Locate every leukocyte (white blood cell).
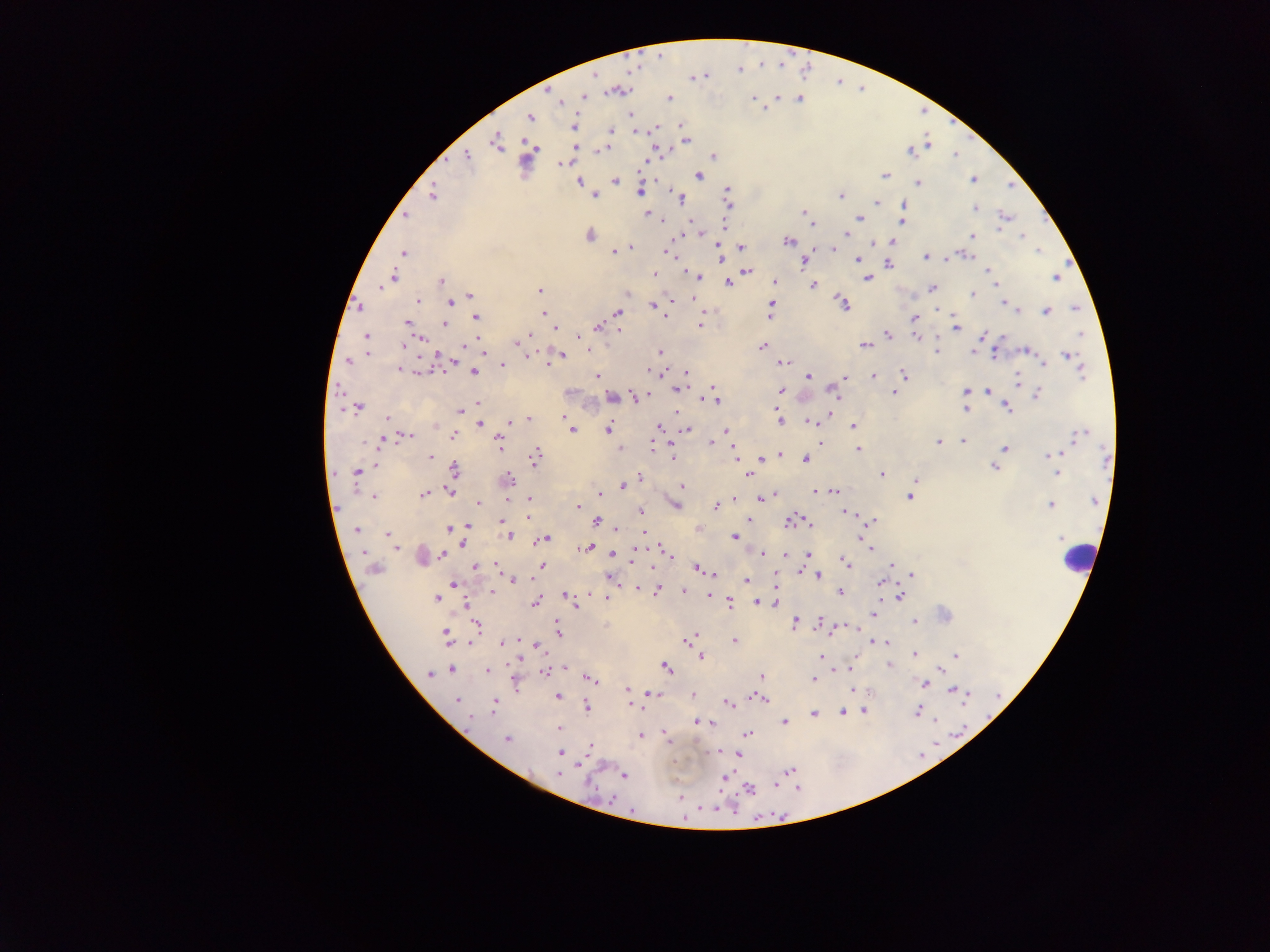
Approximate centers as [x, y] in pixels.
Leukocytes: [1077, 561].

Plasmodium parasite locations: [593, 75], [705, 75], [839, 81], [610, 90], [621, 91], [669, 98], [583, 99], [752, 99], [798, 99], [560, 102], [625, 112], [530, 117], [679, 124], [574, 125], [657, 127], [610, 130], [687, 140], [497, 143], [926, 146], [536, 148], [604, 148], [910, 153], [956, 156], [466, 157], [646, 161], [564, 163], [699, 175], [885, 176], [616, 180], [972, 180], [579, 181], [918, 182], [1010, 188], [726, 191], [638, 192], [433, 194], [591, 194], [676, 194], [839, 196], [680, 197], [877, 204], [906, 204], [973, 208], [803, 210], [646, 215], [406, 218], [860, 218], [1007, 218], [690, 220], [726, 221], [902, 223], [703, 234], [845, 234], [591, 235], [680, 236], [969, 236], [1020, 236], [711, 237], [789, 242], [892, 242], [742, 247], [666, 249], [833, 249], [622, 250], [1038, 252], [402, 254], [924, 257], [720, 258], [952, 258], [858, 260], [804, 261], [889, 264], [988, 269], [657, 271], [749, 272], [699, 276], [393, 277], [867, 279], [1054, 279], [775, 282], [445, 283], [995, 283], [727, 284], [813, 286], [380, 289], [933, 289], [539, 290], [470, 295], [973, 295], [694, 298], [416, 300], [671, 301], [450, 302], [771, 304], [1003, 304], [843, 305], [655, 307], [1074, 307], [358, 308], [939, 309], [544, 312], [1046, 312], [1019, 313], [617, 314], [703, 315], [476, 317], [913, 320], [409, 323], [446, 323], [701, 325], [597, 328], [956, 328], [557, 329], [622, 329], [888, 334], [531, 335], [982, 336], [368, 337], [579, 337], [917, 338], [422, 339], [517, 342], [864, 344], [762, 345], [464, 347], [592, 350], [660, 352], [935, 352], [1026, 352], [367, 354], [973, 354], [1067, 354], [482, 355], [530, 355], [560, 356], [997, 357], [438, 359], [783, 362], [1042, 363], [349, 364], [503, 364], [400, 369], [647, 371], [473, 372], [686, 372], [414, 373], [1081, 373], [903, 374], [808, 377], [873, 378], [601, 379], [842, 379], [1019, 379], [712, 386], [678, 390], [781, 390], [895, 390], [832, 392], [969, 392], [987, 392], [1037, 393], [611, 396], [635, 397], [837, 401], [717, 402], [479, 404], [1007, 407], [361, 408], [461, 410], [774, 410], [964, 410], [565, 416], [386, 418], [528, 418], [830, 418], [478, 423], [780, 424], [435, 425], [509, 425], [809, 425], [570, 426], [852, 426], [659, 427], [608, 431], [687, 431], [727, 431], [1077, 433], [409, 435], [453, 435], [709, 440], [963, 440], [939, 441], [498, 442], [821, 442], [654, 448], [859, 448], [1004, 449], [1064, 451], [431, 454], [734, 454], [1056, 454], [782, 456], [1047, 457], [536, 458], [674, 458], [762, 458], [805, 459], [377, 466], [993, 467], [452, 469], [356, 473], [750, 473], [883, 473], [1058, 473], [640, 477], [509, 478], [915, 481], [682, 486], [623, 487], [357, 489], [815, 490], [451, 492], [601, 492], [835, 493], [429, 494], [372, 496], [528, 498], [909, 498], [735, 499], [509, 500], [760, 500], [1092, 501], [677, 504], [1052, 504], [716, 505], [479, 506], [577, 507], [640, 512], [849, 513], [503, 519], [527, 519], [749, 520], [873, 520], [792, 521], [597, 523], [468, 526], [807, 526], [356, 529], [449, 529], [618, 529], [861, 531], [645, 532], [385, 535], [734, 536], [510, 537], [545, 538], [1058, 538], [540, 540], [464, 545], [591, 548], [397, 549], [868, 550], [764, 552], [613, 553], [771, 553], [807, 553], [666, 554], [442, 555], [784, 556], [633, 558], [670, 558], [890, 564], [542, 566], [845, 567], [476, 569], [697, 570], [811, 572], [713, 573], [910, 576], [818, 577], [774, 579], [746, 581], [512, 582], [454, 584], [880, 584], [637, 587], [657, 588], [684, 591], [491, 592], [565, 592], [840, 593], [438, 597], [709, 597], [900, 598], [607, 599], [756, 600], [730, 602], [536, 604], [464, 605], [573, 606], [874, 615], [794, 620], [820, 622], [915, 623], [478, 626], [559, 628], [833, 633], [445, 634], [446, 636], [693, 636], [735, 641], [871, 642], [887, 643], [501, 644], [537, 646], [820, 655], [915, 655], [957, 655], [701, 657], [889, 664], [666, 666], [566, 668], [451, 670], [487, 670], [838, 671], [544, 674], [431, 675], [761, 676], [591, 679], [813, 680], [924, 683], [627, 684], [851, 689], [952, 691], [628, 693], [649, 694], [557, 696], [762, 699], [455, 702], [729, 703], [632, 707], [587, 709], [863, 709], [915, 710], [813, 713], [845, 713], [696, 722], [784, 722], [469, 723], [559, 727], [640, 735], [747, 735], [507, 739], [589, 746], [561, 754], [740, 756], [581, 767], [787, 771], [558, 772], [624, 774], [728, 777], [776, 784], [589, 785], [748, 790]. Thick blood film. Mobile-phone photograph taken through the microscope. Sample from Ghana. Image is 1270×952 pixels. Single field of view.